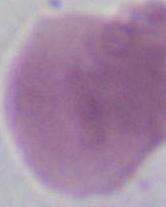
Captured at 1000x magnification. An erythrocyte is shown. Micrograph.